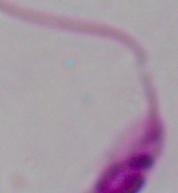 A Leishmania parasite is shown. Photomicrograph. Captured at 1000x magnification.